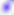
Toxoplasma gondii is seen. 400x magnification. Micrograph.